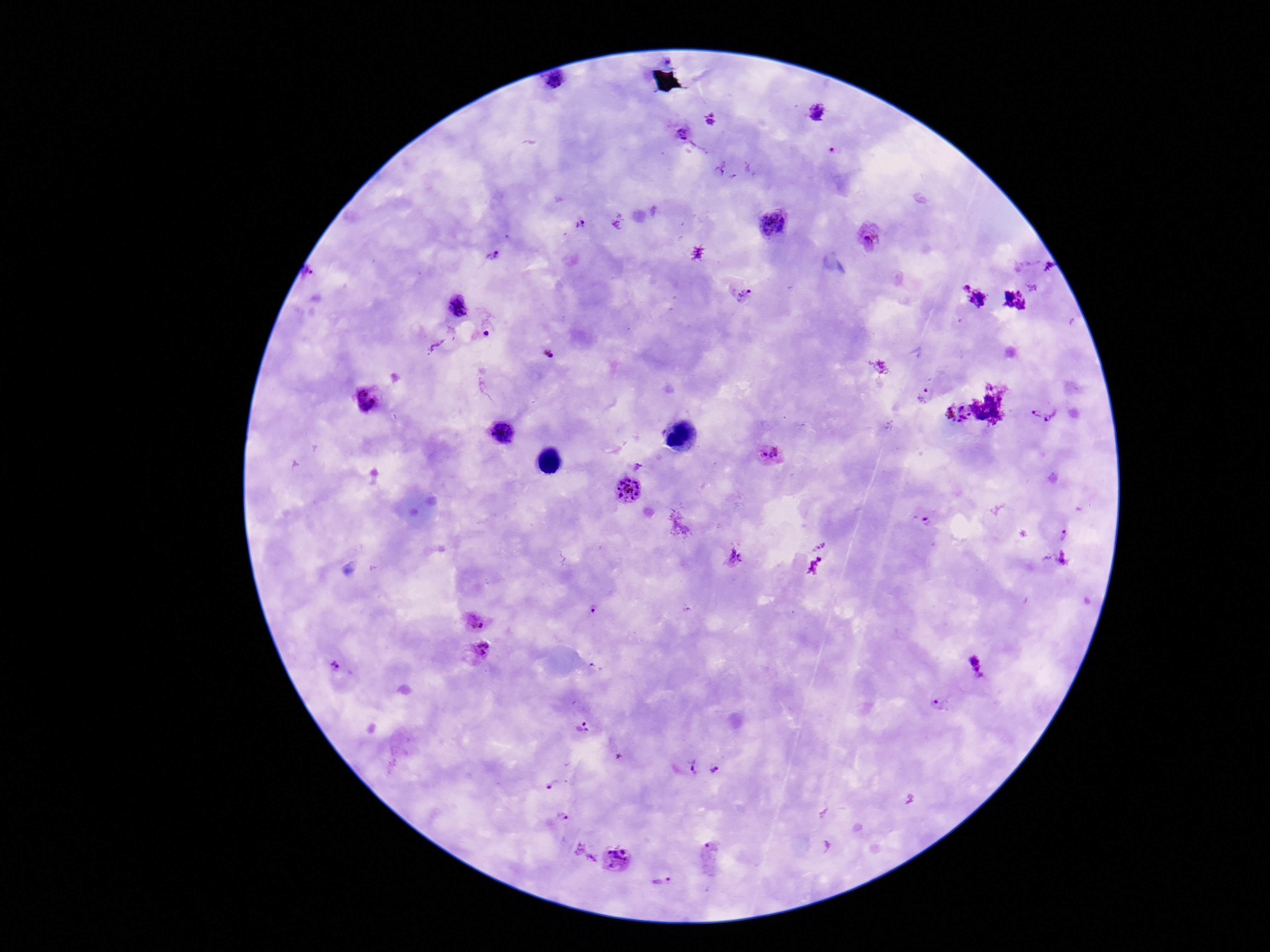
Approximate object centers, in pixels from the top-left corner.
Summary:
  - Plasmodium parasite locations: (x=557, y=82), (x=817, y=113), (x=682, y=134), (x=773, y=224), (x=870, y=238), (x=493, y=256), (x=745, y=297), (x=457, y=306), (x=486, y=334), (x=547, y=354), (x=924, y=395), (x=364, y=401), (x=957, y=414), (x=1037, y=415), (x=1052, y=416), (x=502, y=433), (x=769, y=456), (x=639, y=465), (x=627, y=489), (x=926, y=523), (x=1063, y=533), (x=735, y=558), (x=593, y=611), (x=476, y=622), (x=482, y=649), (x=975, y=666), (x=336, y=667), (x=940, y=703), (x=584, y=728), (x=693, y=766), (x=715, y=770), (x=549, y=787), (x=564, y=816), (x=710, y=854), (x=617, y=859), (x=662, y=880)
  - Magnification: 100x
  - Stain: Giemsa
  - Image size: 1270×952 pixels
  - Preparation: thick blood film
  - Patient malaria status: infected
  - Field of view: single
  - Capture: smartphone camera through the microscope eyepiece